State which parasite is depicted.
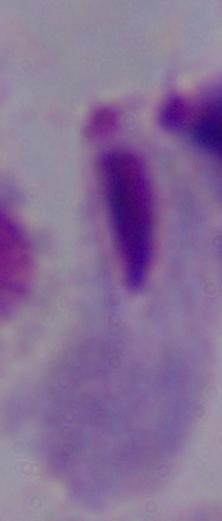

This is a trichomonad.

Summary:
  - Modality: micrograph
  - Magnification: 1000x